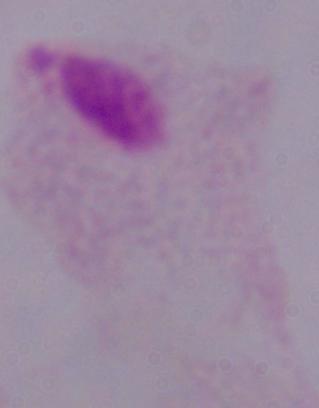

Summary:
  - Identification: trichomonad
  - Modality: photomicrograph
  - Magnification: 1000x